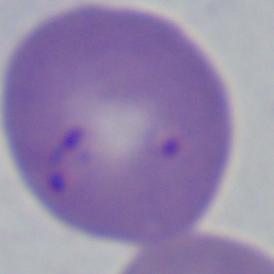 Captured at 1000x magnification. A Babesia parasite is shown. Photomicrograph.